Comment on the morphology of the erythrocytes.
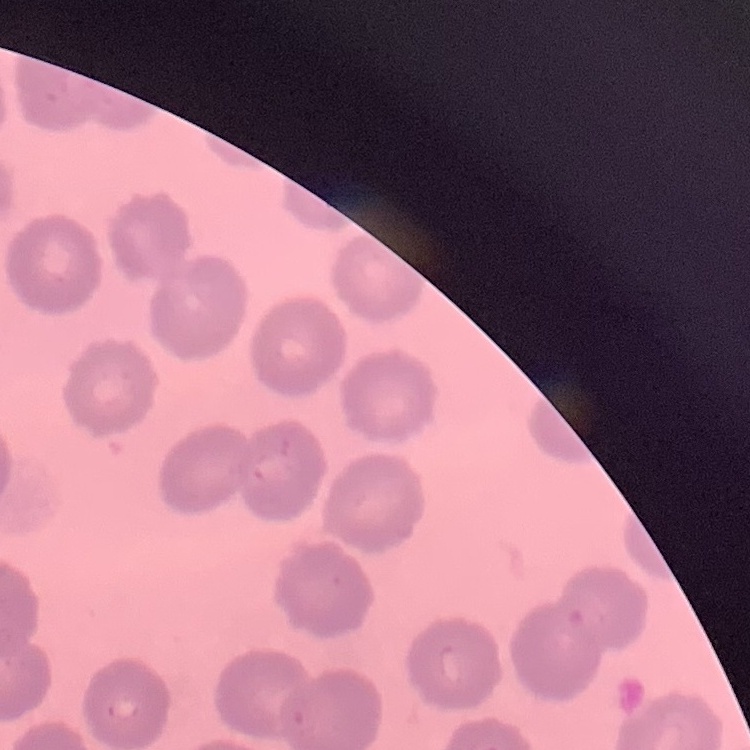

They show no rouleaux formation.

{
  "preparation": "thin blood smear",
  "stain": "Field's or Giemsa",
  "image_type": "square crop of a larger photomicrograph"
}